Comment on the background quality.
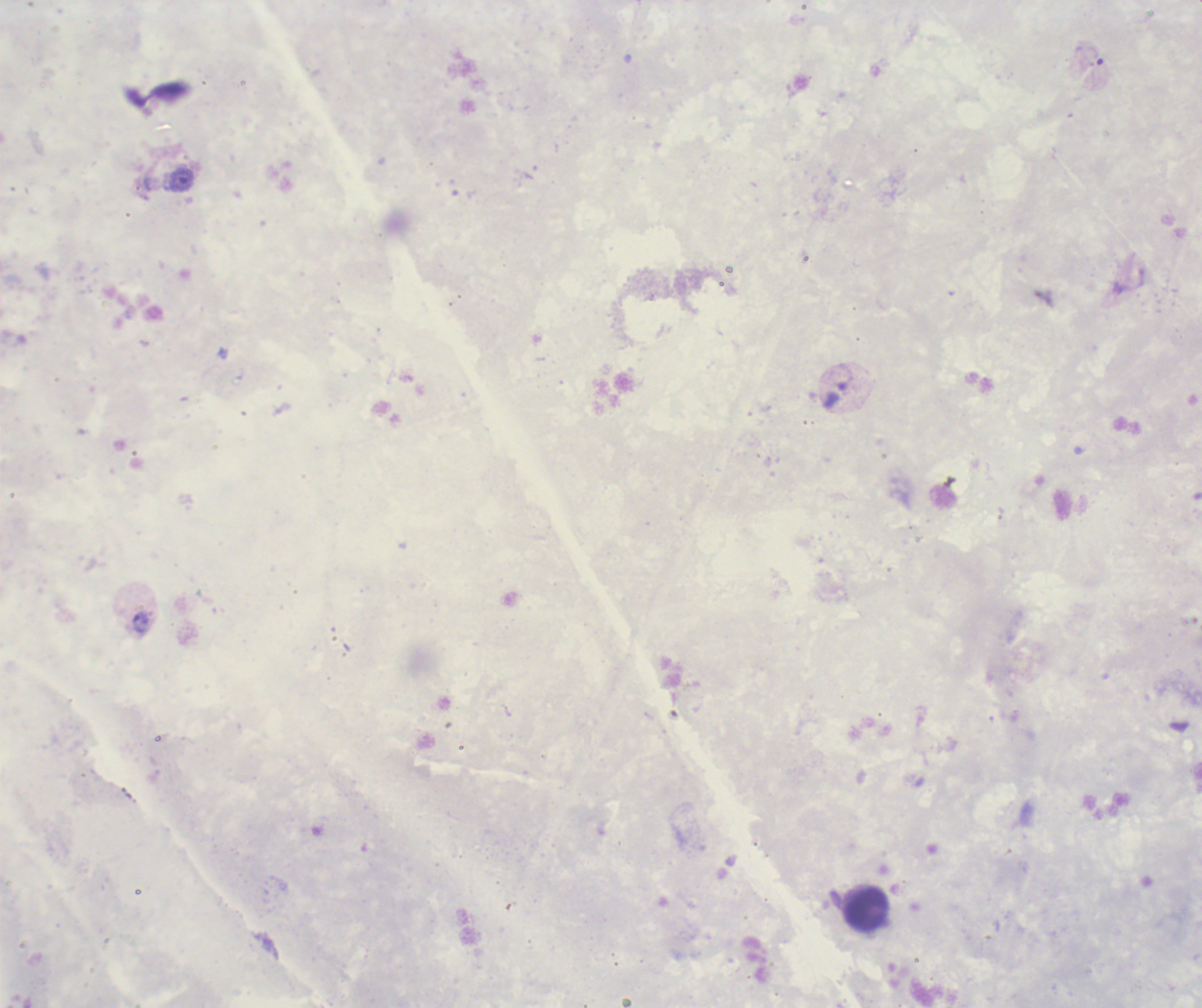

Poor.

Approximate object centers, in pixels from the top-left corner. Trophozoite locations: (x=1094, y=57), (x=182, y=180), (x=140, y=623). Leukocyte locations: (x=866, y=910). Previously used in an actual diagnosis. Thick blood smear. Romanowsky stain. Result: positive for malaria parasites. Image is 1202×1008 pixels. Captured at 100x magnification. Single field of view.